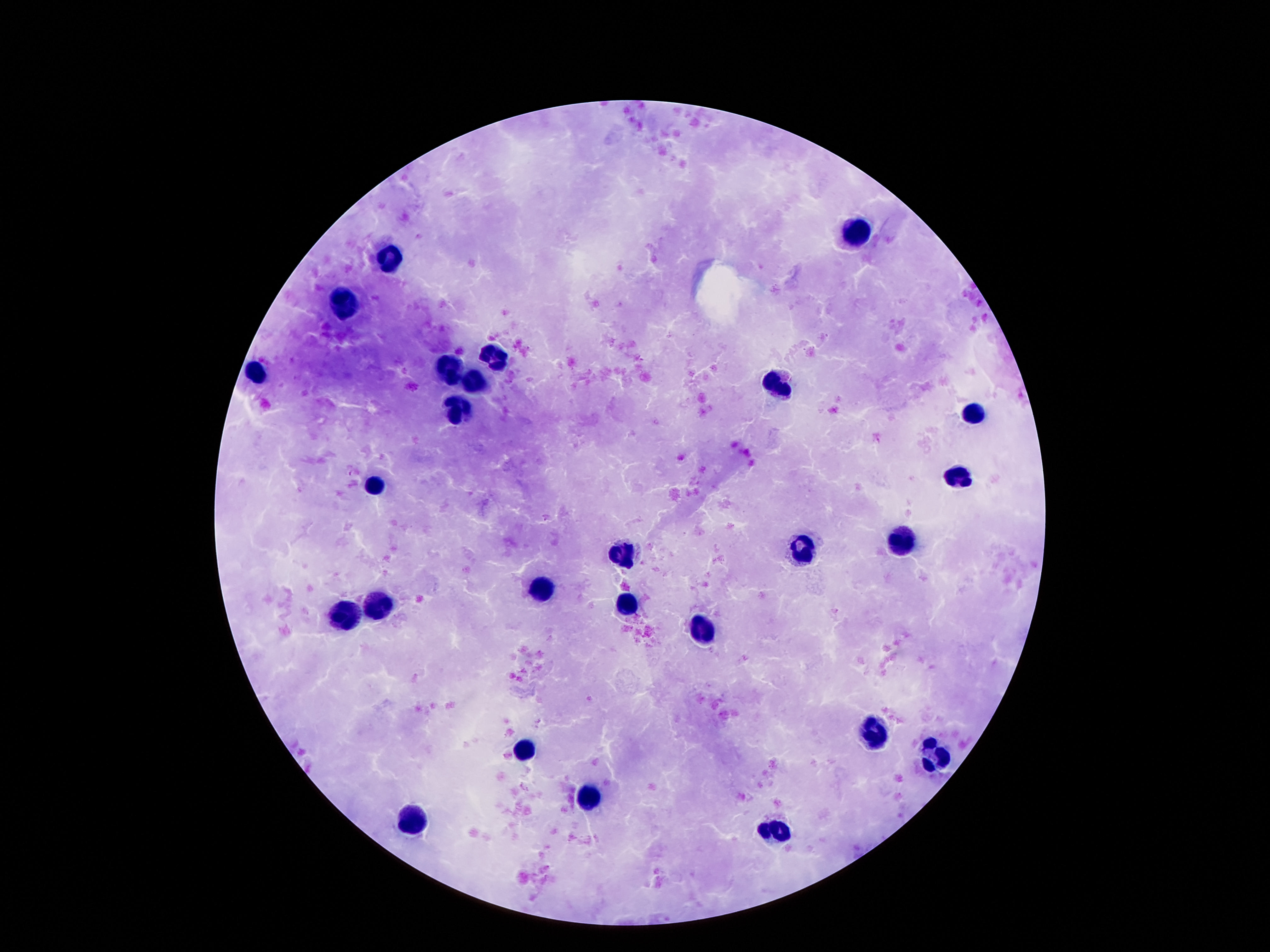

preparation = thick peripheral-blood smear
leukocyte locations = approximate centers as {x, y} in pixels: {859, 236}, {389, 258}, {346, 299}, {492, 358}, {451, 370}, {254, 375}, {473, 379}, {779, 383}, {457, 410}, {973, 412}, {957, 475}, {371, 485}, {902, 543}, {799, 550}, {625, 553}, {545, 590}, {379, 603}, {629, 605}, {342, 614}, {703, 631}, {873, 734}, {527, 747}, {932, 758}, {584, 798}, {416, 816}, {779, 833}
patient malaria status = not infected
stain = Giemsa
field of view = one from this slide
capture = smartphone camera through the microscope eyepiece
image size = 1270×952 pixels
magnification = 100x